State which parasite is depicted.
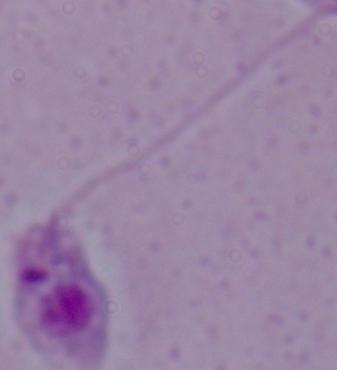

This is Leishmania.

Micrograph. 1000x magnification.